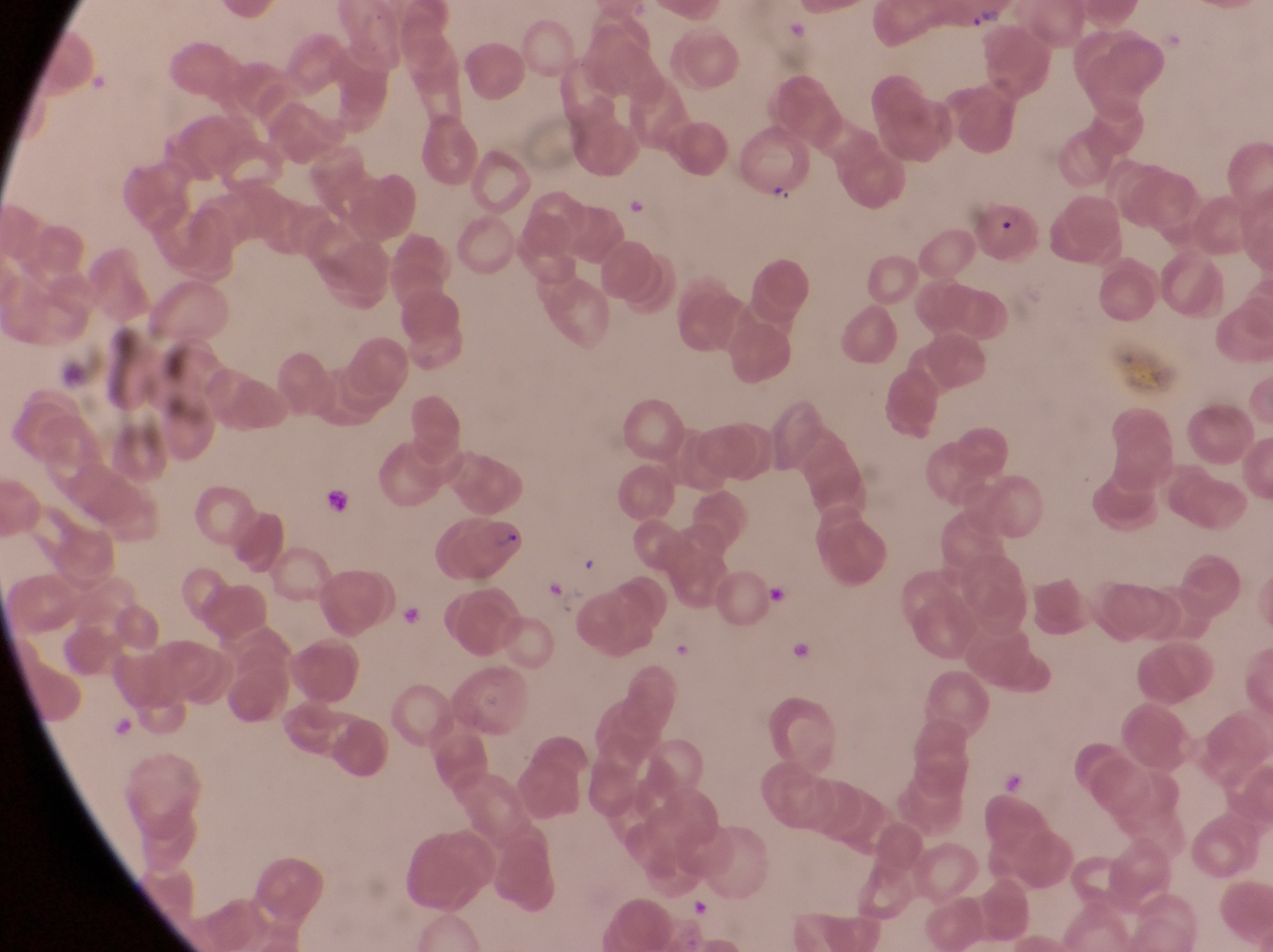

Approximate bounding boxes as {left, top, right, bottom} in pixels.
Summary:
  - Artifact (platelet-like body, stain precipitate, or debris) locations: {319, 487, 347, 529}, {543, 576, 564, 603}, {766, 580, 793, 612}, {397, 603, 423, 630}, {785, 636, 814, 664}
  - Parasitised red blood cell locations: {969, 190, 1047, 267}, {426, 509, 525, 592}
  - Trophozoite locations: {764, 180, 792, 210}, {619, 187, 647, 220}
  - Preparation: thin blood smear
  - Capture: smartphone photograph through the eyepiece of an Olympus CX-23 microscope
  - Field of view: single
  - Magnification: 1000x
  - Image size: 1273×952 pixels
  - Country: Uganda